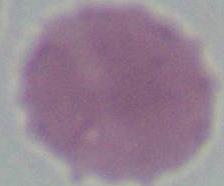
Summary:
  - Modality: micrograph
  - Magnification: 1000x
  - Identification: red blood cell